Describe the morphology of the red blood cells.
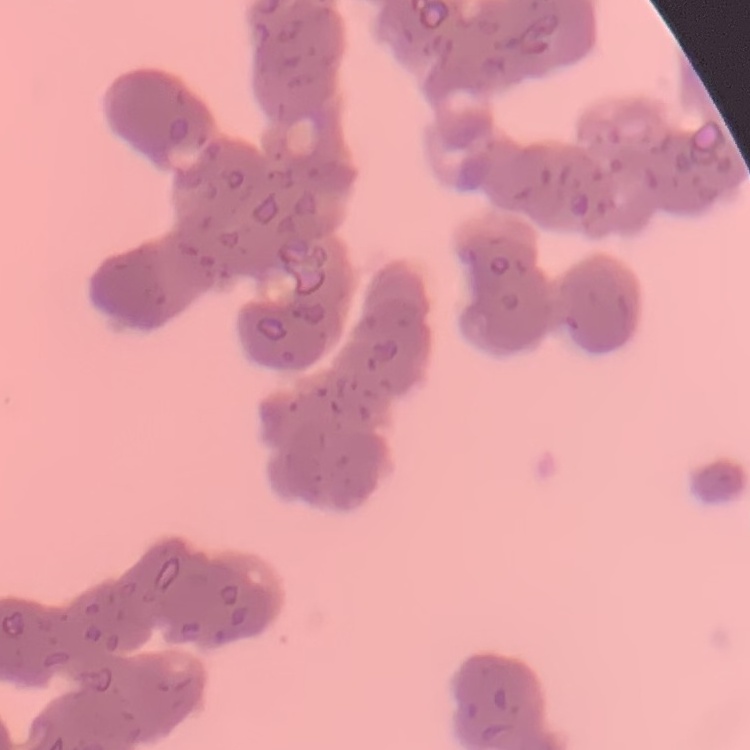
Rouleaux formation.

{
  "image_type": "square crop of a larger photomicrograph",
  "stain": "Field's or Giemsa",
  "preparation": "thin blood film"
}